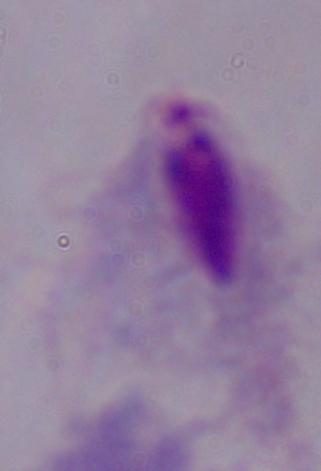

Summary:
  - Modality: micrograph
  - Magnification: 1000x
  - Identification: trichomonad